Assess this cell for malaria.
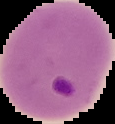
Parasitized.

{
  "image_type": "segmented cell region on a black background",
  "preparation": "thin blood smear",
  "image_size": "115×124 pixels"
}